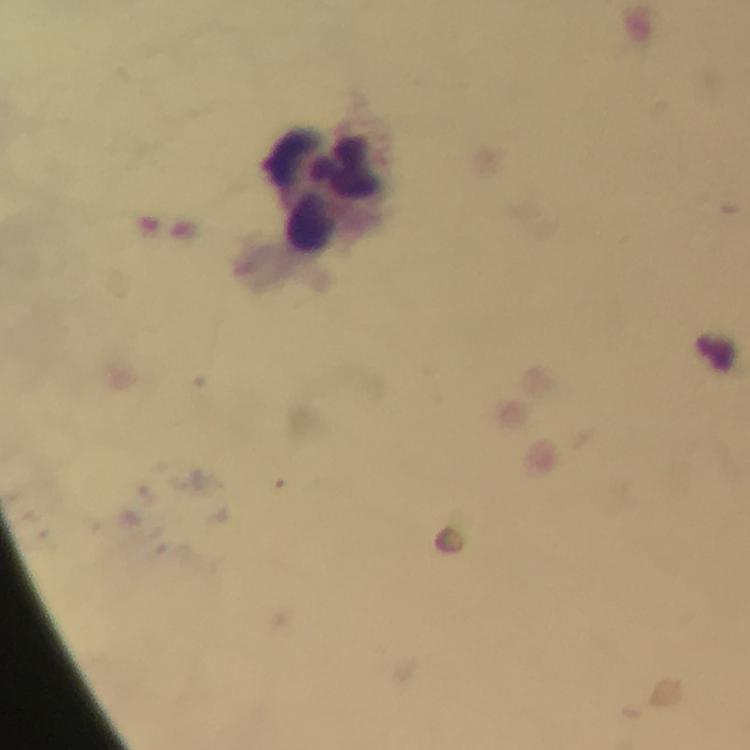

cropped from = one field of view
image size = 750×750 pixels
stain = Giemsa
magnification = 100x
leukocyte locations = approximate object centers, in pixels from the top-left corner: (x=326, y=185)
preparation = thick smear
immersion oil = applied
capture = smartphone camera through the microscope
malaria parasites = none seen
context = from a diagnostic examination for malaria